Point out each malaria parasite and each leukocyte.
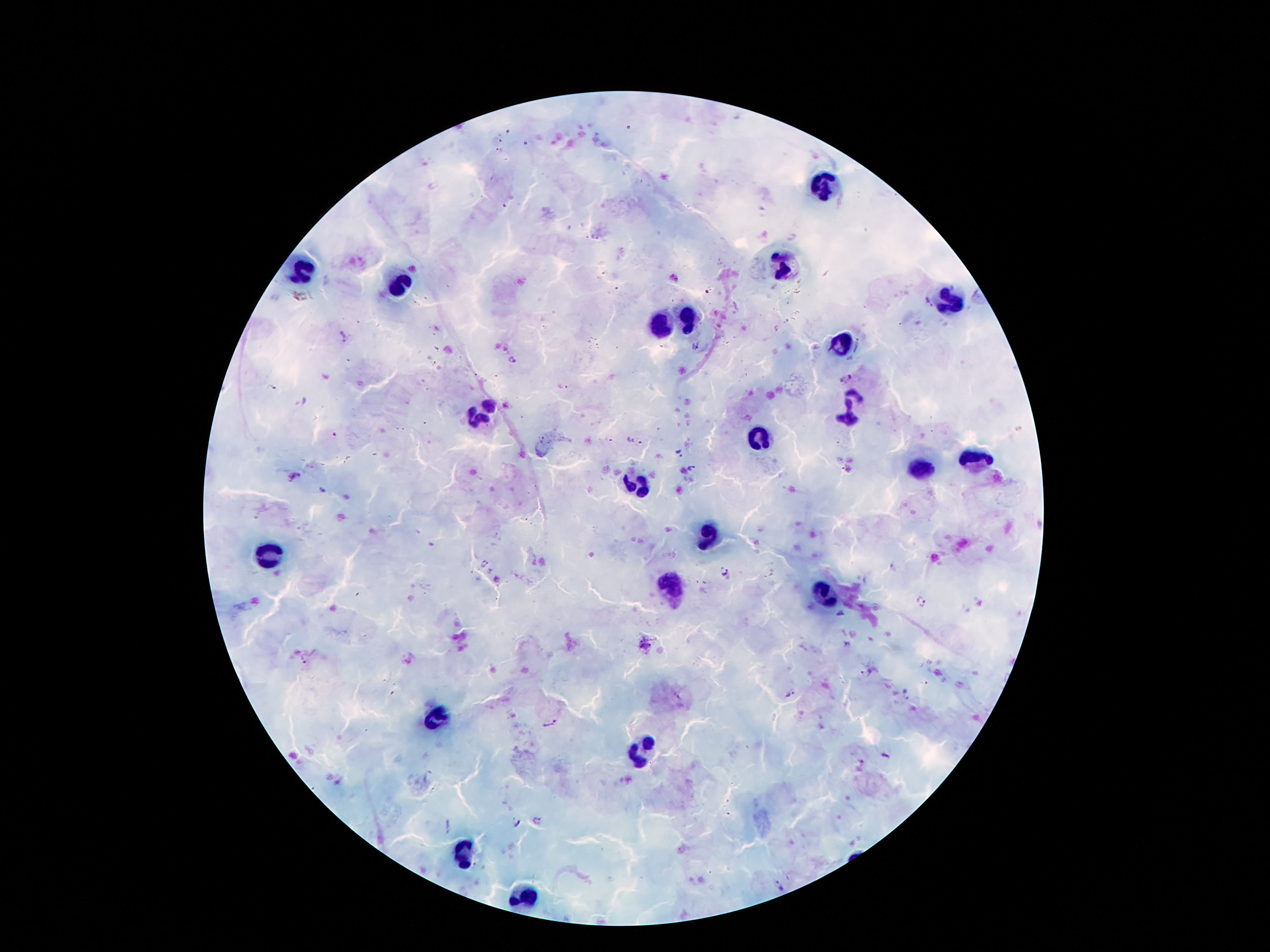
Approximate centers as [x, y] in pixels.
Malaria parasites: [674, 278], [343, 337], [512, 360], [845, 377], [678, 453], [692, 469], [295, 476], [320, 491], [484, 563], [725, 572], [921, 601], [840, 614], [306, 657], [866, 674], [790, 693], [549, 724], [885, 755], [516, 821], [536, 821], [778, 885].
Leukocytes: [826, 187], [779, 263], [301, 271], [397, 284], [949, 302], [689, 317], [660, 328], [840, 347], [849, 407], [481, 416], [759, 439], [971, 462], [912, 466], [631, 483], [706, 533], [267, 555], [670, 584], [824, 594], [435, 718], [639, 752], [462, 851], [525, 897].

Photographed through the microscope eyepiece with a smartphone camera. One field from this slide. Patient malaria status: infected with Plasmodium falciparum. Giemsa-stained preparation. Thick blood film. 100x magnification. Image is 1270×952 pixels.